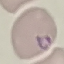

Summary:
  - Malaria status: parasitized
  - Stain: Giemsa
  - Capture: smartphone through the microscope eyepiece
  - Image type: cell patch, automatically extracted from a larger field of view and resized to 64 × 64 pixels
  - Preparation: thin smear